Assess this cell for malaria.
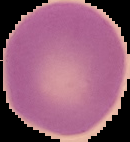

It is uninfected.

preparation: thin blood film
image_type: segmented cell region on a black background
image_size: 130×142 pixels